Outline each uninfected red blood cell.
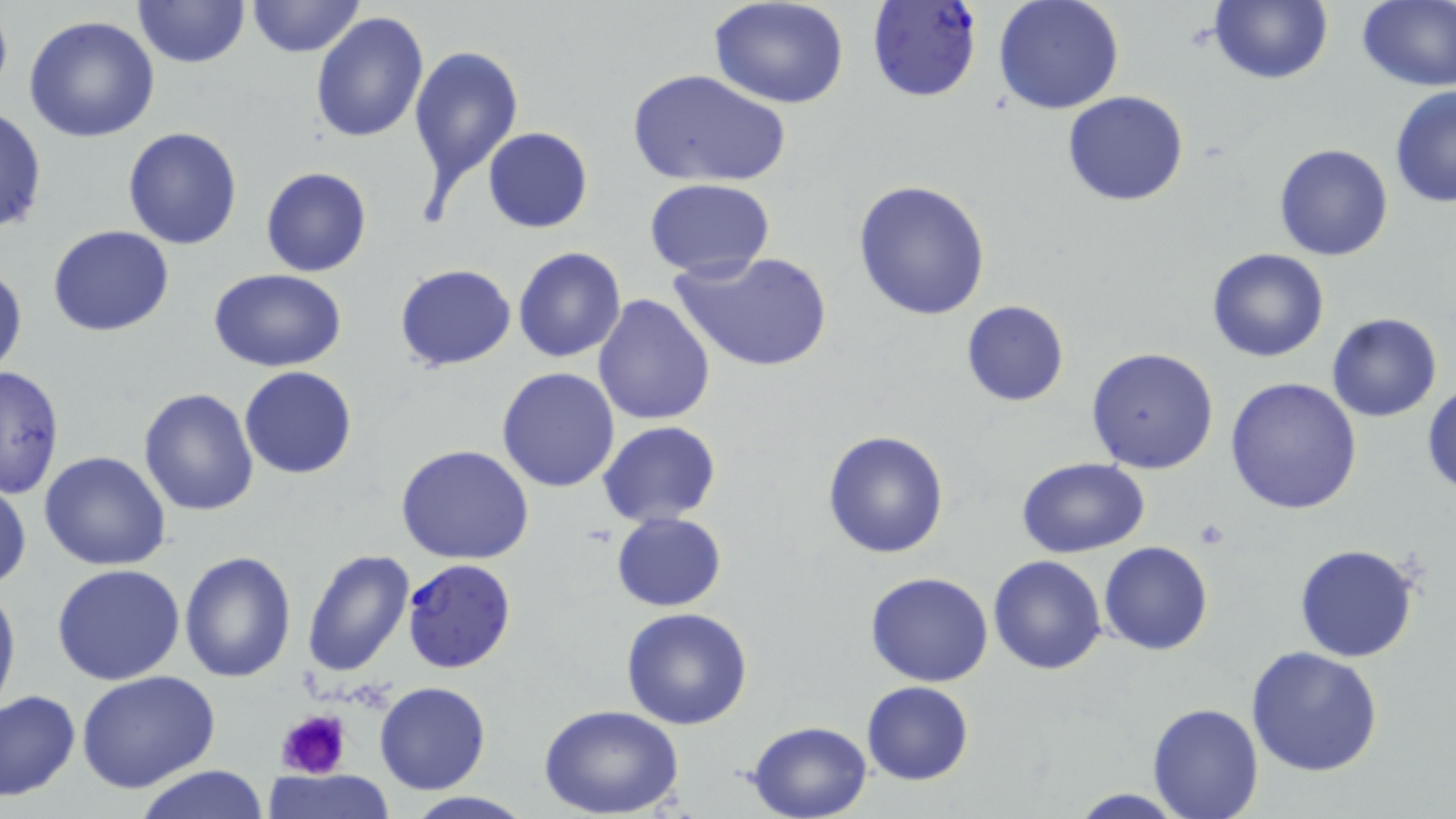
Approximate bounding boxes as [x1, y1, x2, y2] in pixels.
Uninfected red blood cells: [132, 0, 250, 69], [247, 0, 364, 58], [1356, 0, 1456, 91], [993, 1, 1125, 115], [1209, 1, 1331, 85], [710, 2, 850, 109], [311, 12, 428, 142], [22, 15, 160, 143], [408, 43, 523, 205], [624, 68, 791, 190], [1389, 87, 1455, 209], [1061, 91, 1189, 207], [0, 104, 46, 238], [120, 126, 243, 251], [481, 126, 594, 233], [1272, 142, 1395, 261], [260, 166, 372, 278], [644, 178, 775, 279], [852, 180, 993, 322], [47, 224, 175, 338], [512, 247, 626, 364], [672, 249, 833, 374], [1208, 249, 1330, 363], [0, 262, 26, 380], [394, 263, 516, 373], [208, 269, 347, 374], [591, 293, 716, 426], [961, 301, 1070, 407], [1326, 314, 1442, 422], [1086, 347, 1219, 474], [0, 364, 65, 498], [239, 367, 359, 479], [496, 368, 621, 492], [1224, 377, 1363, 515], [1424, 385, 1456, 495], [138, 387, 261, 517], [597, 419, 722, 526], [821, 428, 950, 560], [394, 444, 536, 565], [39, 452, 171, 571], [1014, 457, 1150, 559], [0, 478, 30, 594], [611, 511, 727, 612], [1099, 541, 1213, 655], [1294, 542, 1421, 662], [180, 550, 298, 685], [300, 550, 416, 678], [989, 555, 1108, 674], [52, 562, 186, 684], [864, 571, 993, 686], [0, 573, 20, 720], [621, 607, 753, 731], [1245, 645, 1386, 777], [75, 669, 221, 793], [373, 681, 491, 796], [861, 681, 974, 785], [0, 688, 81, 801], [1148, 702, 1264, 818], [538, 703, 686, 819], [745, 720, 875, 818], [133, 765, 271, 819], [265, 769, 392, 819], [1066, 789, 1193, 819], [397, 792, 538, 819].

Plasmodium falciparum-infected red blood cell locations: [866, 3, 984, 105], [401, 558, 518, 674]. Platelet locations: [275, 708, 351, 782]. Slide-level diagnosis: Plasmodium falciparum. Thin blood film. One field of a larger specimen. Captured at 1000x magnification. Image is 1456×819 pixels. May-Grünwald-Giemsa stain. Optical microscopy.